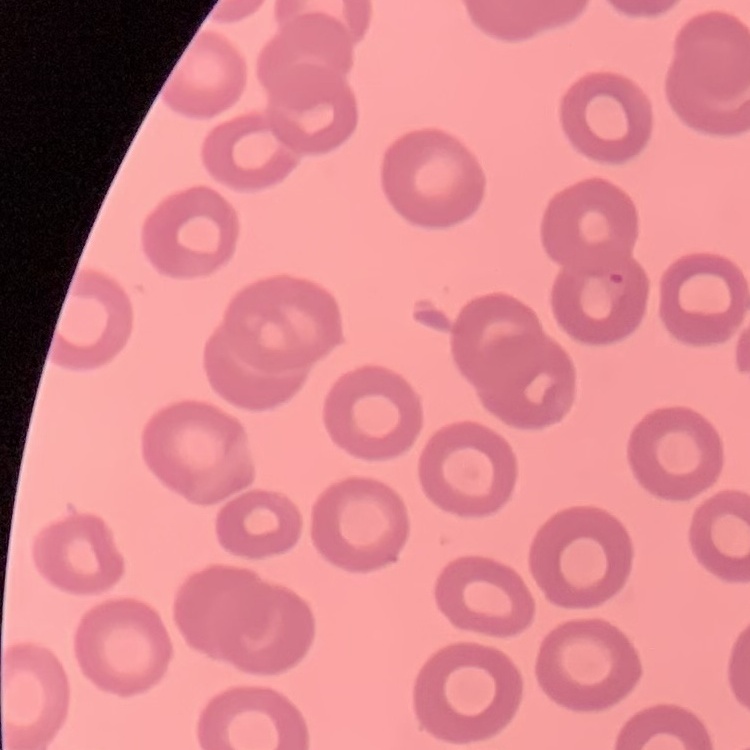

erythrocyte_morphology: no rouleaux formation
preparation: thin blood film
image_type: square crop of a larger photomicrograph
stain: Field's or Giemsa